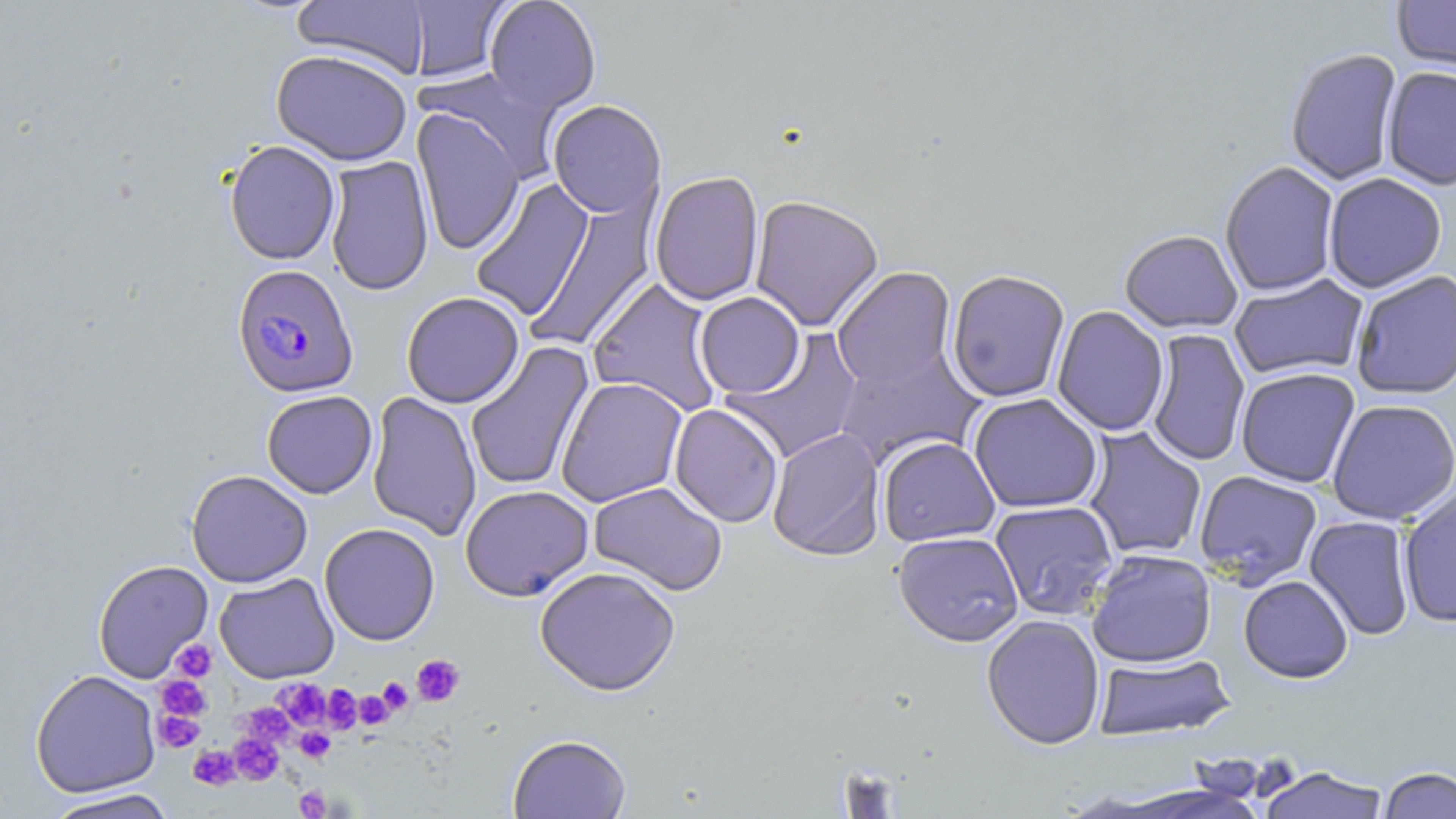
Approximate bounding boxes as named x1/y1/x2/y2 corners in pixels. Uninfected red blood cell locations: (x1=291, y1=0, x2=431, y2=79), (x1=403, y1=0, x2=512, y2=83), (x1=484, y1=0, x2=601, y2=113), (x1=1392, y1=0, x2=1456, y2=78), (x1=459, y1=35, x2=599, y2=164), (x1=271, y1=49, x2=413, y2=166), (x1=1285, y1=49, x2=1403, y2=187), (x1=420, y1=67, x2=566, y2=183), (x1=1382, y1=68, x2=1456, y2=192), (x1=548, y1=100, x2=666, y2=220), (x1=411, y1=107, x2=525, y2=255), (x1=224, y1=140, x2=341, y2=265), (x1=325, y1=155, x2=435, y2=297), (x1=1220, y1=162, x2=1340, y2=297), (x1=650, y1=171, x2=765, y2=306), (x1=1323, y1=174, x2=1447, y2=295), (x1=470, y1=178, x2=595, y2=321), (x1=525, y1=194, x2=658, y2=353), (x1=749, y1=195, x2=884, y2=332), (x1=1120, y1=231, x2=1243, y2=334), (x1=832, y1=267, x2=957, y2=391), (x1=947, y1=269, x2=1070, y2=404), (x1=1351, y1=271, x2=1456, y2=400), (x1=1229, y1=274, x2=1368, y2=381), (x1=587, y1=277, x2=723, y2=416), (x1=401, y1=291, x2=524, y2=408), (x1=694, y1=293, x2=806, y2=399), (x1=1052, y1=306, x2=1169, y2=437), (x1=1146, y1=329, x2=1250, y2=466), (x1=723, y1=330, x2=864, y2=463), (x1=465, y1=340, x2=595, y2=492), (x1=833, y1=344, x2=985, y2=469), (x1=1236, y1=368, x2=1361, y2=488), (x1=556, y1=377, x2=688, y2=507), (x1=262, y1=390, x2=378, y2=498), (x1=366, y1=391, x2=482, y2=540), (x1=968, y1=393, x2=1103, y2=514), (x1=1327, y1=399, x2=1456, y2=525), (x1=669, y1=403, x2=783, y2=528), (x1=1083, y1=426, x2=1207, y2=560), (x1=767, y1=428, x2=885, y2=561), (x1=878, y1=436, x2=1000, y2=546), (x1=186, y1=469, x2=313, y2=587), (x1=1195, y1=470, x2=1322, y2=588), (x1=588, y1=481, x2=727, y2=596), (x1=460, y1=485, x2=594, y2=601), (x1=1398, y1=488, x2=1456, y2=628), (x1=990, y1=500, x2=1118, y2=620), (x1=1304, y1=515, x2=1416, y2=641), (x1=319, y1=523, x2=440, y2=645), (x1=893, y1=531, x2=1024, y2=647), (x1=1086, y1=550, x2=1217, y2=668), (x1=92, y1=560, x2=214, y2=683), (x1=535, y1=566, x2=681, y2=696), (x1=214, y1=572, x2=339, y2=683), (x1=1238, y1=576, x2=1353, y2=684), (x1=981, y1=614, x2=1105, y2=750), (x1=1092, y1=652, x2=1236, y2=743), (x1=30, y1=669, x2=161, y2=798), (x1=508, y1=734, x2=631, y2=819), (x1=1257, y1=766, x2=1390, y2=819), (x1=1379, y1=767, x2=1456, y2=818), (x1=43, y1=788, x2=176, y2=819). Plasmodium falciparum-infected red blood cell locations: (x1=232, y1=264, x2=359, y2=398). Platelet locations: (x1=171, y1=638, x2=217, y2=682), (x1=411, y1=654, x2=465, y2=706), (x1=155, y1=675, x2=211, y2=722), (x1=377, y1=677, x2=413, y2=715), (x1=275, y1=678, x2=330, y2=729), (x1=321, y1=685, x2=362, y2=734), (x1=353, y1=690, x2=394, y2=729), (x1=239, y1=702, x2=295, y2=747), (x1=153, y1=707, x2=206, y2=751), (x1=295, y1=727, x2=336, y2=764), (x1=230, y1=733, x2=284, y2=784), (x1=190, y1=745, x2=239, y2=789), (x1=294, y1=785, x2=331, y2=818). Slide-level diagnosis: Plasmodium falciparum. Image is 1456×819 pixels. Optical microscopy. Captured at 1000x magnification. May-Grünwald-Giemsa stain. Thin blood smear. Single field of view.